Report the malaria status.
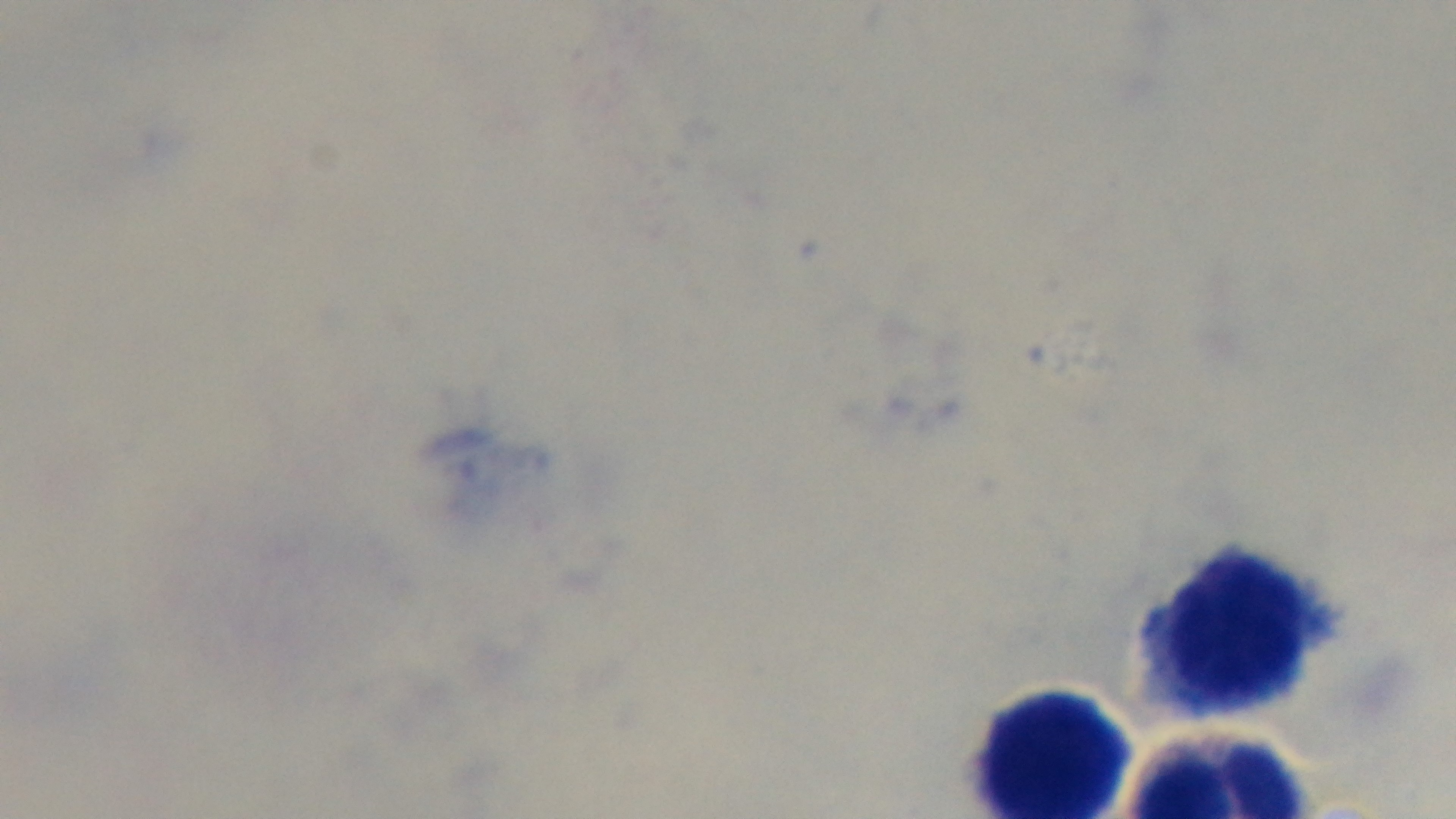

It is uninfected.

Giemsa-stained. 100x oil-immersion objective. Preparation: thick. Mounted 4K digital camera. Single field of view. Light microscopy.